Classify the preparation.
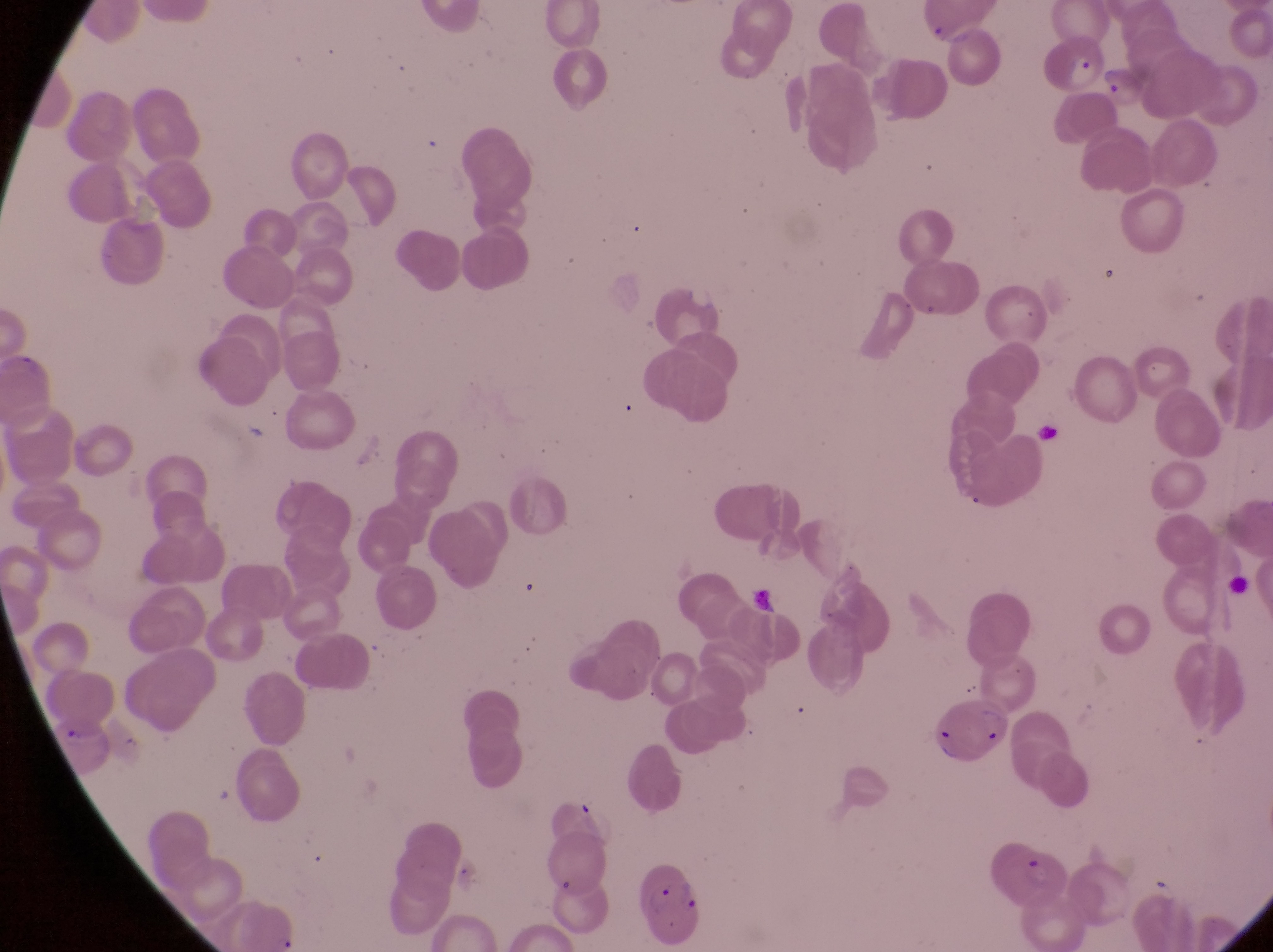
Thin blood film.

Approximate bounding boxes as left top right bottom in pixels. Parasitised red blood cell locations: 1045 32 1102 93; 928 704 1015 767; 976 829 1071 906; 635 863 705 943. Single field of view. Sample from Uganda. Image is 1273×952 pixels. Captured by a smartphone held over the eyepiece of an Olympus CX-23 microscope. Magnification of 1000x.